Classify this cell by malaria status.
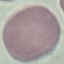

Uninfected.

{
  "stain": "Giemsa",
  "image_type": "cell patch, automatically extracted from a larger field of view and resized to 64 × 64 pixels",
  "capture": "smartphone through the microscope eyepiece",
  "preparation": "thin smear"
}